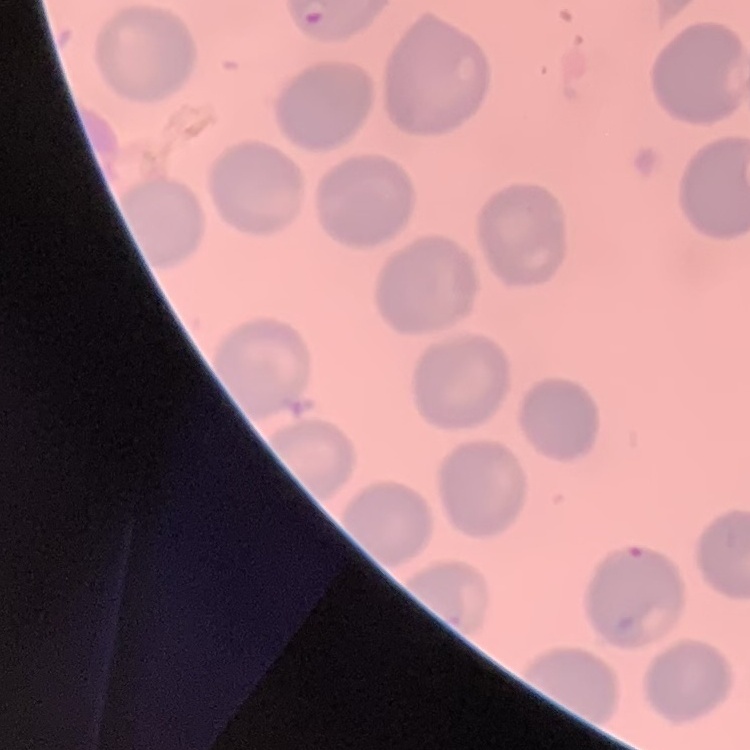
The red blood cells show no rouleaux formation. Field's or Giemsa stain. Square crop of a larger photomicrograph. Thin peripheral smear.